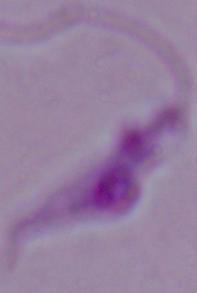
{
  "magnification": "1000x",
  "modality": "micrograph",
  "identification": "Leishmania"
}